Identify the parasite.
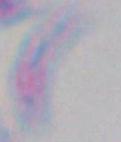
Toxoplasma gondii.

Micrograph. Captured at 1000x magnification.